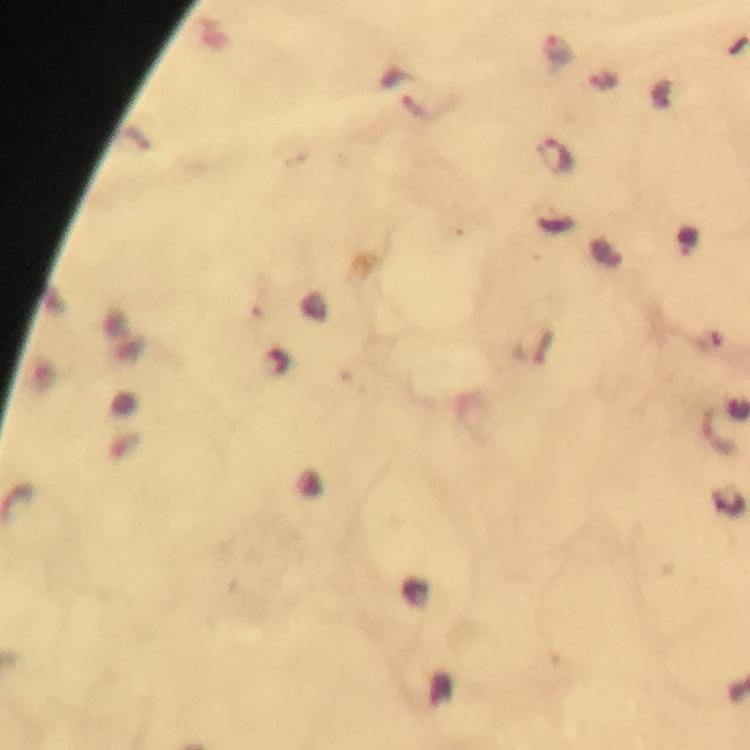

Approximate centers as (x, y) in pixels.
Summary:
  - Plasmodium parasite locations: (556, 50), (602, 80), (554, 153), (718, 430)
  - Stain: Giemsa
  - Preparation: thick blood smear
  - Capture: smartphone mounted on the microscope
  - Context: from a malaria diagnostic workup
  - Cropped from: a single field of view
  - Image size: 750×750 pixels
  - Magnification: 100x
  - Immersion oil: applied